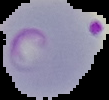 Image is 109×100 pixels. Segmented cell region on a black background. Malaria status: parasitized. From a thin blood film.